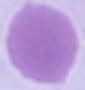

{
  "modality": "micrograph",
  "magnification": "1000x",
  "identification": "erythrocyte"
}